Report the malaria status of this cell.
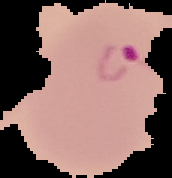

Parasitized.

Summary:
  - Image size: 172×178 pixels
  - Image type: cell region segmented out of the field of view; surrounding area masked to black
  - Preparation: thin blood film